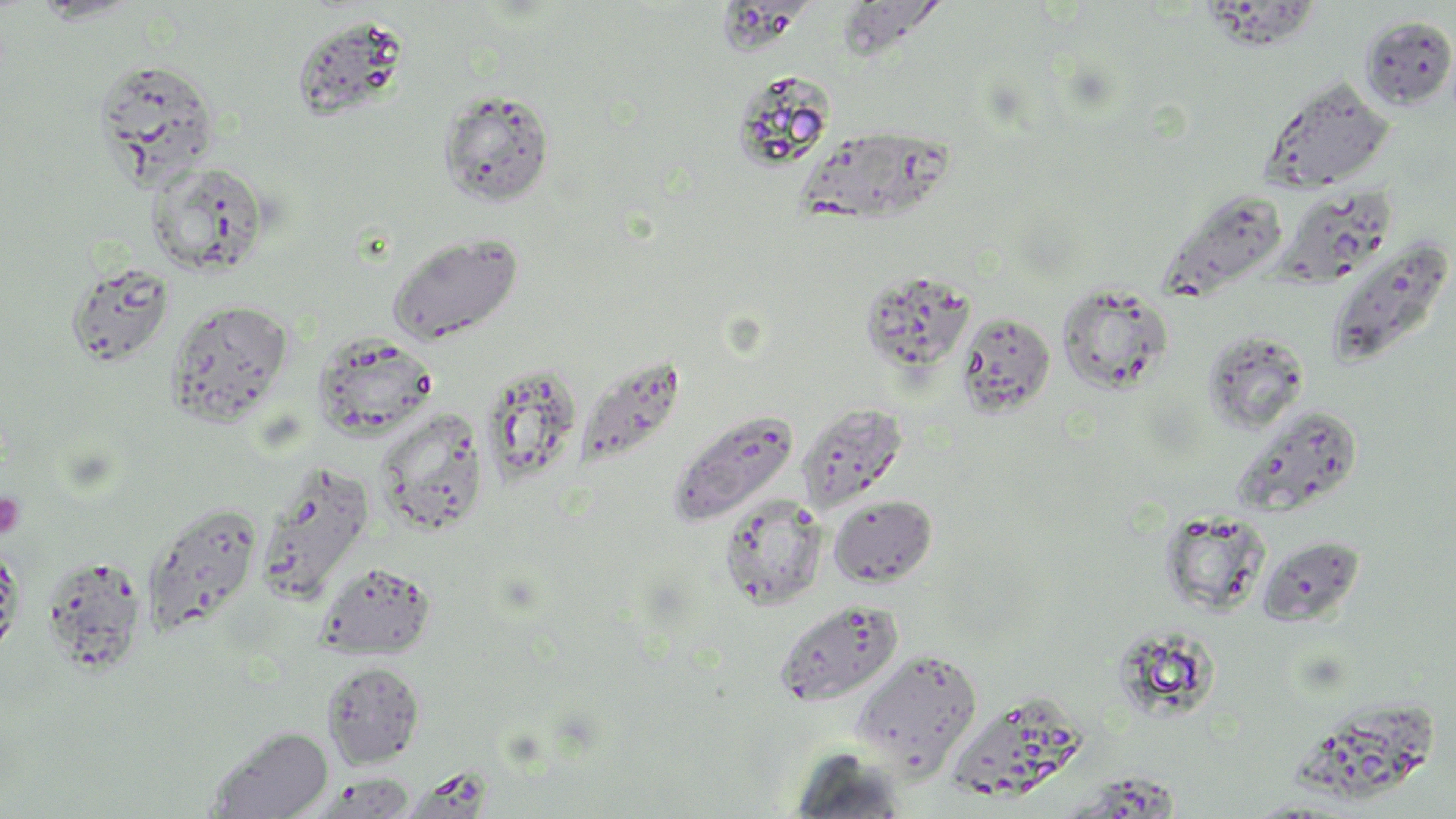 Approximate bounding boxes as named x1/y1/x2/y2 corners in pixels. Uninfected red blood cell locations: (x1=29, y1=0, x2=142, y2=23), (x1=715, y1=0, x2=803, y2=57), (x1=1196, y1=3, x2=1318, y2=52), (x1=837, y1=5, x2=942, y2=64), (x1=1358, y1=14, x2=1456, y2=111), (x1=290, y1=15, x2=409, y2=123), (x1=94, y1=59, x2=219, y2=185), (x1=731, y1=70, x2=837, y2=171), (x1=1260, y1=75, x2=1396, y2=193), (x1=437, y1=88, x2=556, y2=208), (x1=791, y1=131, x2=959, y2=226), (x1=145, y1=160, x2=272, y2=278), (x1=1276, y1=184, x2=1397, y2=289), (x1=1157, y1=188, x2=1291, y2=302), (x1=386, y1=231, x2=524, y2=345), (x1=1324, y1=236, x2=1455, y2=368), (x1=65, y1=260, x2=176, y2=369), (x1=860, y1=269, x2=977, y2=377), (x1=1057, y1=284, x2=1174, y2=395), (x1=165, y1=299, x2=294, y2=427), (x1=955, y1=310, x2=1056, y2=420), (x1=1197, y1=328, x2=1314, y2=434), (x1=313, y1=333, x2=438, y2=441), (x1=574, y1=352, x2=687, y2=473), (x1=480, y1=363, x2=584, y2=488), (x1=797, y1=402, x2=908, y2=512), (x1=1234, y1=406, x2=1364, y2=518), (x1=668, y1=408, x2=802, y2=528), (x1=376, y1=409, x2=489, y2=536), (x1=254, y1=461, x2=375, y2=604), (x1=718, y1=493, x2=829, y2=611), (x1=828, y1=495, x2=937, y2=587), (x1=142, y1=501, x2=263, y2=638), (x1=1158, y1=511, x2=1271, y2=616), (x1=1257, y1=534, x2=1365, y2=626), (x1=0, y1=539, x2=24, y2=663), (x1=39, y1=554, x2=149, y2=677), (x1=316, y1=561, x2=436, y2=660), (x1=774, y1=599, x2=903, y2=707), (x1=1115, y1=625, x2=1223, y2=719), (x1=851, y1=648, x2=983, y2=776), (x1=322, y1=661, x2=425, y2=768), (x1=946, y1=696, x2=1090, y2=805), (x1=1292, y1=699, x2=1444, y2=798), (x1=207, y1=725, x2=333, y2=819), (x1=785, y1=747, x2=912, y2=817), (x1=308, y1=774, x2=416, y2=818). Platelet locations: (x1=0, y1=492, x2=26, y2=539). Slide-level diagnosis: negative for blood parasites. Light microscopy. Thin blood smear. Image is 1456×819 pixels. May-Grünwald-Giemsa stain. 1000x magnification. One field of a larger specimen.